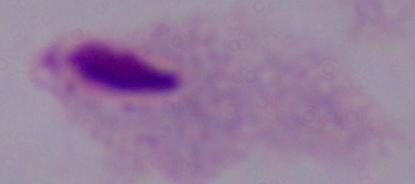

modality: micrograph
magnification: 1000x
identification: trichomonad